Comment on the morphology of the erythrocytes.
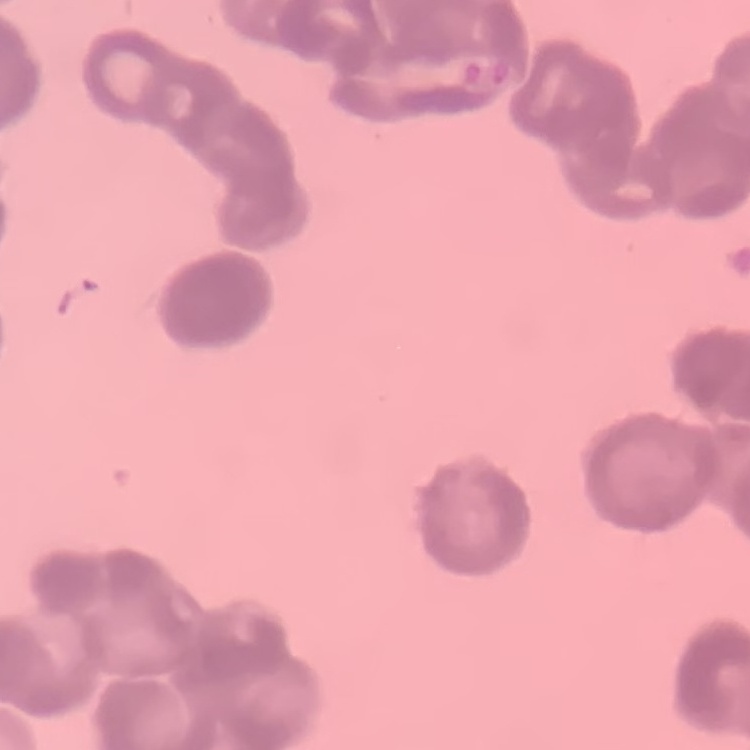

They show rouleaux formation.

Stained with either Field's or Giemsa. Square crop of a larger photomicrograph. Thin peripheral smear.